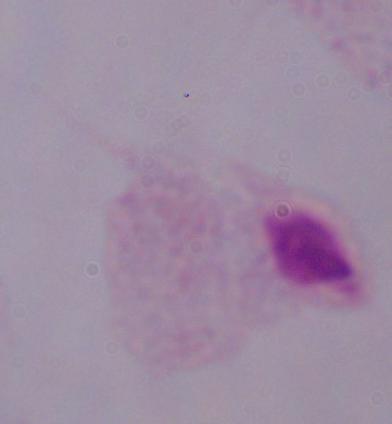
magnification: 1000x
identification: trichomonad
modality: micrograph